Outline each blood parasite and name the species.
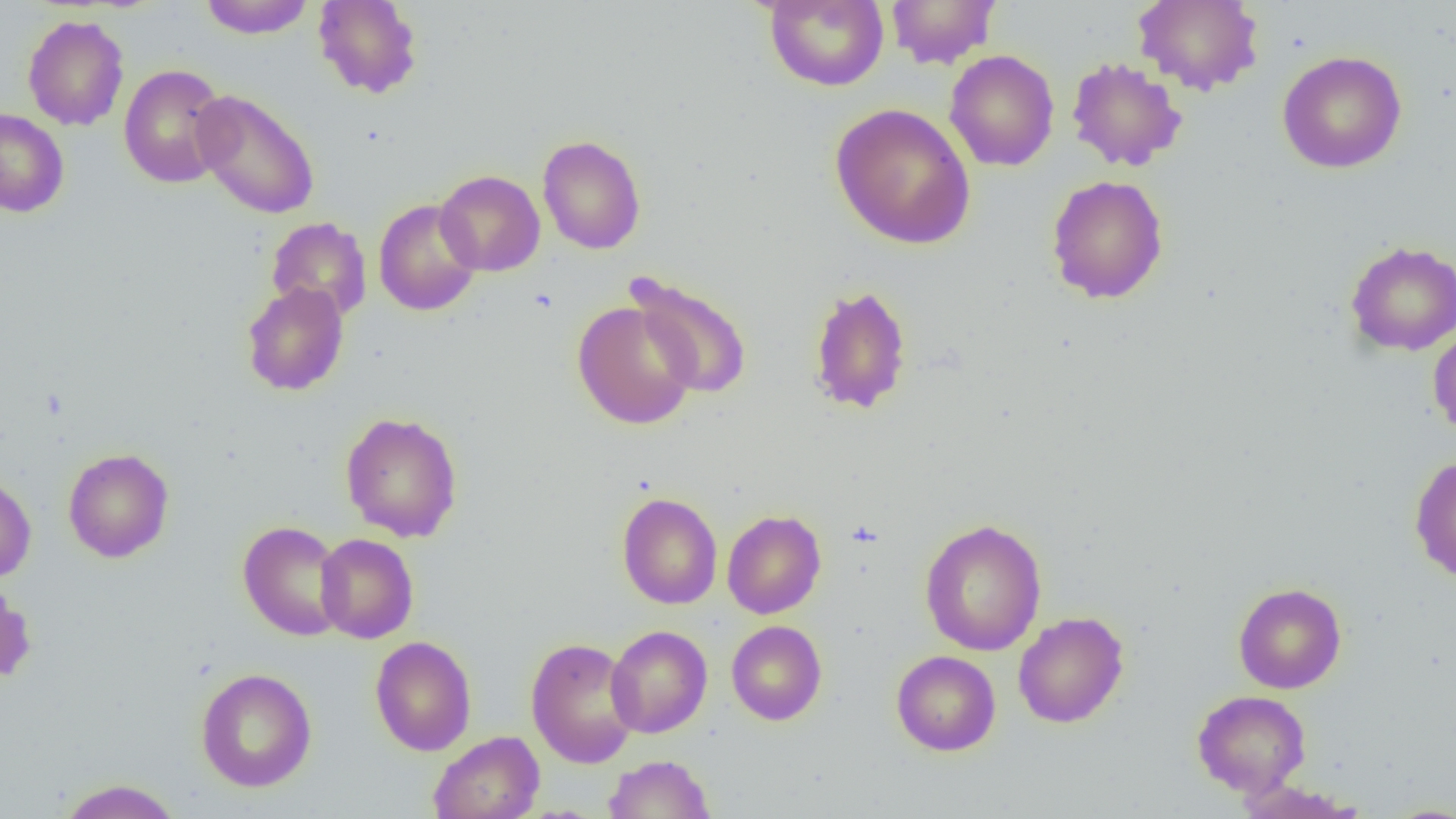
No blood parasites observed.

Approximate bounding boxes as named x1/y1/x2/y2 corners in pixels. Uninfected red blood cell locations: (x1=199, y1=0, x2=315, y2=38), (x1=313, y1=0, x2=423, y2=99), (x1=764, y1=0, x2=889, y2=91), (x1=885, y1=0, x2=1001, y2=69), (x1=1133, y1=1, x2=1264, y2=96), (x1=22, y1=14, x2=129, y2=131), (x1=945, y1=49, x2=1059, y2=172), (x1=1277, y1=50, x2=1407, y2=173), (x1=1066, y1=56, x2=1187, y2=172), (x1=118, y1=63, x2=232, y2=189), (x1=191, y1=89, x2=320, y2=220), (x1=830, y1=102, x2=976, y2=250), (x1=0, y1=108, x2=69, y2=217), (x1=537, y1=134, x2=647, y2=254), (x1=435, y1=169, x2=545, y2=277), (x1=1046, y1=175, x2=1169, y2=304), (x1=373, y1=198, x2=482, y2=316), (x1=266, y1=217, x2=372, y2=321), (x1=1345, y1=240, x2=1456, y2=355), (x1=627, y1=274, x2=753, y2=401), (x1=241, y1=281, x2=349, y2=396), (x1=808, y1=284, x2=913, y2=415), (x1=572, y1=300, x2=699, y2=431), (x1=1427, y1=324, x2=1456, y2=438), (x1=340, y1=411, x2=464, y2=542), (x1=62, y1=447, x2=175, y2=563), (x1=1409, y1=454, x2=1456, y2=583), (x1=0, y1=470, x2=36, y2=583), (x1=617, y1=492, x2=723, y2=609), (x1=722, y1=510, x2=826, y2=619), (x1=919, y1=518, x2=1047, y2=656), (x1=237, y1=520, x2=348, y2=641), (x1=315, y1=533, x2=418, y2=644), (x1=0, y1=580, x2=37, y2=685), (x1=1233, y1=583, x2=1346, y2=693), (x1=1013, y1=611, x2=1129, y2=728), (x1=726, y1=620, x2=827, y2=725), (x1=606, y1=625, x2=712, y2=738), (x1=370, y1=635, x2=477, y2=756), (x1=525, y1=637, x2=640, y2=768), (x1=890, y1=650, x2=1001, y2=756), (x1=195, y1=668, x2=317, y2=792), (x1=1191, y1=690, x2=1311, y2=797), (x1=429, y1=731, x2=544, y2=819), (x1=604, y1=754, x2=716, y2=818), (x1=56, y1=779, x2=184, y2=818), (x1=1235, y1=779, x2=1366, y2=819), (x1=1378, y1=803, x2=1456, y2=818). Slide-level diagnosis: negative for blood parasites. Thin blood smear. Captured at 1000x magnification. Single field of view. Image is 1456×819 pixels. Optical microscopy.